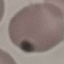
Malaria status: uninfected. Thin blood film. Photographed with a smartphone camera at the microscope eyepiece. Cell patch, automatically extracted from a larger field of view and resized to 64 × 64 pixels. Giemsa stain.